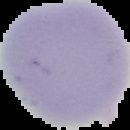

Image is 130×130 pixels. Result: negative for Plasmodium parasites. From a thin blood film. Cell region segmented out of the field of view; the surrounding area is masked to black.